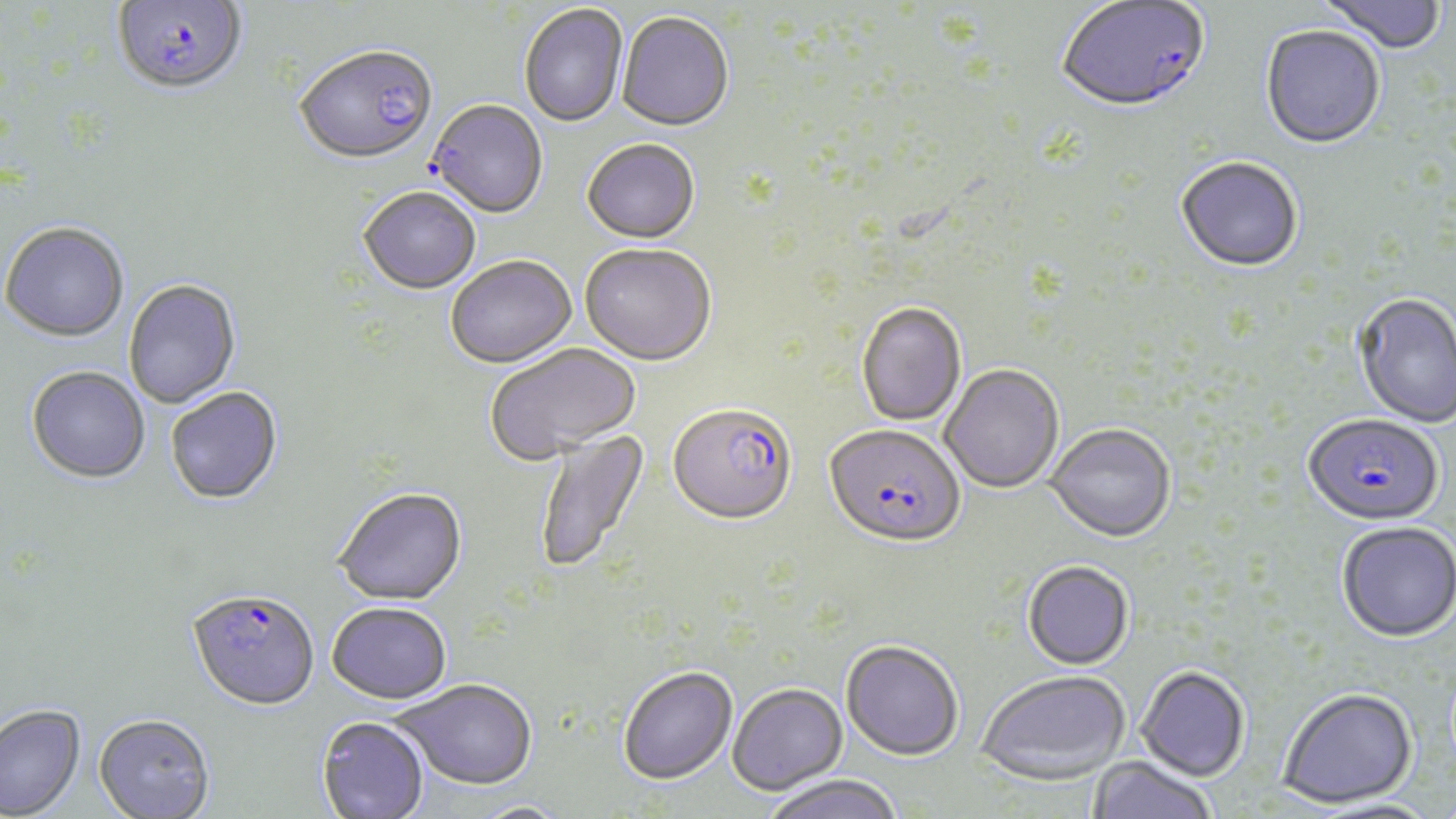 Approximate bounding boxes as named x1/y1/x2/y2 corners in pixels. Uninfected red blood cell locations: (x1=1316, y1=0, x2=1447, y2=57), (x1=519, y1=5, x2=628, y2=129), (x1=617, y1=14, x2=733, y2=134), (x1=1260, y1=27, x2=1386, y2=151), (x1=294, y1=49, x2=438, y2=168), (x1=427, y1=101, x2=549, y2=220), (x1=582, y1=141, x2=700, y2=246), (x1=1176, y1=159, x2=1303, y2=274), (x1=358, y1=190, x2=481, y2=296), (x1=1, y1=222, x2=130, y2=342), (x1=580, y1=246, x2=716, y2=368), (x1=446, y1=258, x2=577, y2=371), (x1=123, y1=279, x2=241, y2=409), (x1=1353, y1=295, x2=1456, y2=428), (x1=857, y1=304, x2=967, y2=427), (x1=486, y1=344, x2=642, y2=464), (x1=26, y1=366, x2=150, y2=483), (x1=940, y1=366, x2=1064, y2=494), (x1=166, y1=387, x2=283, y2=505), (x1=1047, y1=426, x2=1175, y2=544), (x1=533, y1=429, x2=652, y2=573), (x1=334, y1=489, x2=468, y2=607), (x1=1337, y1=522, x2=1456, y2=642), (x1=1023, y1=561, x2=1134, y2=670), (x1=327, y1=604, x2=452, y2=706), (x1=841, y1=640, x2=964, y2=761), (x1=1136, y1=665, x2=1250, y2=781), (x1=618, y1=666, x2=738, y2=785), (x1=976, y1=670, x2=1130, y2=785), (x1=394, y1=680, x2=538, y2=791), (x1=728, y1=683, x2=848, y2=795), (x1=1277, y1=687, x2=1418, y2=808), (x1=0, y1=704, x2=86, y2=818), (x1=93, y1=713, x2=215, y2=818), (x1=316, y1=716, x2=429, y2=819), (x1=1087, y1=756, x2=1219, y2=819), (x1=762, y1=775, x2=905, y2=819), (x1=1308, y1=797, x2=1443, y2=818), (x1=466, y1=802, x2=573, y2=818). Plasmodium falciparum-infected red blood cell locations: (x1=112, y1=1, x2=247, y2=99), (x1=1056, y1=1, x2=1211, y2=116), (x1=668, y1=405, x2=797, y2=528), (x1=1303, y1=416, x2=1444, y2=528), (x1=825, y1=426, x2=965, y2=550), (x1=186, y1=589, x2=320, y2=712). Slide-level diagnosis: Plasmodium falciparum. Light microscopy. One field of a larger specimen. Thin blood smear. Captured at 1000x magnification. May-Grünwald-Giemsa-stained preparation. Image is 1456×819 pixels.